Outline each Plasmodium falciparum-infected red blood cell.
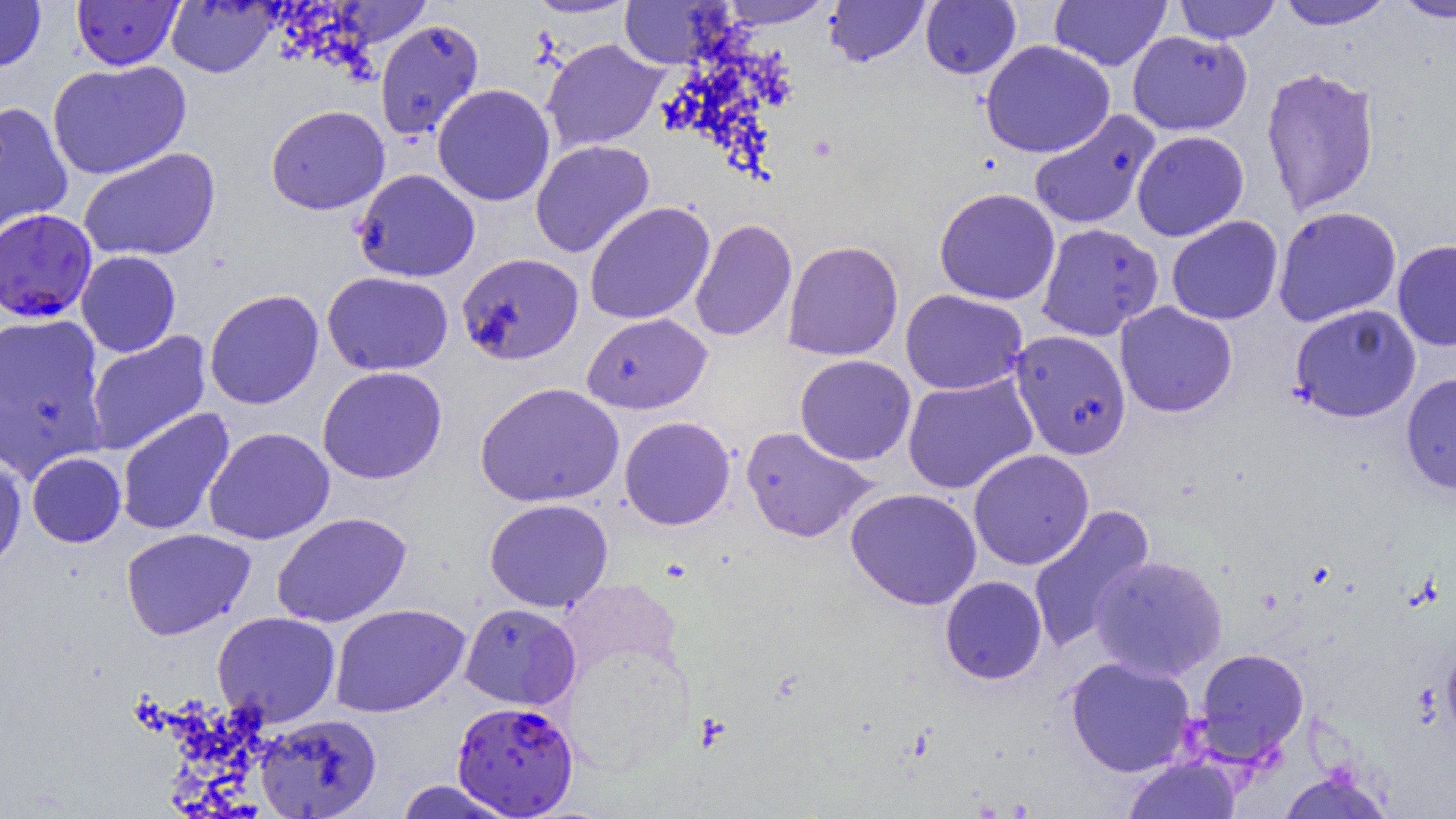
Approximate bounding boxes as [x1, y1, x2, y2] in pixels.
Plasmodium falciparum-infected red blood cells: [0, 208, 97, 323], [452, 700, 579, 817].

{
  "slide_level_diagnosis": "Plasmodium falciparum",
  "uninfected_red_blood_cell_locations": "approximate bounding boxes as [x1, y1, x2, y2] in pixels: [0, 0, 46, 72], [72, 0, 183, 70], [524, 0, 639, 19], [717, 0, 836, 28], [825, 0, 929, 66], [1173, 0, 1281, 43], [1274, 0, 1394, 29], [1391, 0, 1456, 22], [166, 1, 279, 77], [329, 1, 432, 49], [618, 1, 735, 68], [920, 1, 1021, 79], [1050, 1, 1171, 72], [374, 19, 485, 140], [1127, 30, 1252, 135], [541, 38, 667, 152], [980, 39, 1115, 158], [47, 60, 191, 179], [1261, 66, 1380, 217], [432, 84, 555, 206], [0, 101, 73, 237], [266, 105, 390, 215], [1028, 109, 1160, 230], [1132, 130, 1249, 241], [530, 139, 655, 258], [79, 147, 220, 263], [353, 168, 480, 282], [934, 187, 1060, 305], [585, 201, 715, 325], [1273, 206, 1401, 326], [1166, 215, 1283, 325], [689, 219, 797, 342], [1036, 223, 1163, 342], [1393, 239, 1456, 352], [782, 240, 904, 362], [76, 250, 181, 357], [456, 252, 584, 365], [322, 271, 453, 376], [204, 289, 324, 409], [900, 289, 1027, 395], [1115, 302, 1237, 417], [1289, 303, 1421, 422], [0, 312, 107, 475], [581, 312, 712, 415], [85, 330, 211, 456], [1009, 330, 1132, 459], [795, 354, 916, 466], [317, 365, 447, 484], [1400, 372, 1456, 495], [902, 373, 1038, 494], [475, 382, 624, 507], [116, 407, 235, 536], [619, 416, 735, 530], [740, 426, 879, 543], [204, 427, 335, 545], [968, 449, 1094, 570], [0, 450, 27, 572], [26, 451, 126, 547], [845, 487, 982, 610], [484, 498, 613, 612], [1028, 505, 1156, 654], [272, 512, 411, 627], [121, 528, 255, 640], [1091, 555, 1227, 681], [940, 575, 1047, 684], [330, 603, 470, 717], [460, 603, 581, 710], [212, 612, 341, 726], [1442, 639, 1456, 747], [1194, 648, 1309, 764], [1065, 656, 1197, 777], [255, 713, 382, 818], [1124, 757, 1241, 819], [1277, 768, 1395, 818], [393, 779, 519, 819]",
  "field_of_view": "single",
  "magnification": "1000x",
  "preparation": "thin blood film",
  "modality": "optical microscopy",
  "image_size": "1456×819 pixels"
}